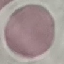
malaria status = uninfected
image type = automatically extracted cell patch, resized to 64 × 64 pixels
capture = smartphone through the microscope eyepiece
preparation = thin smear
stain = Giemsa